Locate every Trypanosoma brucei.
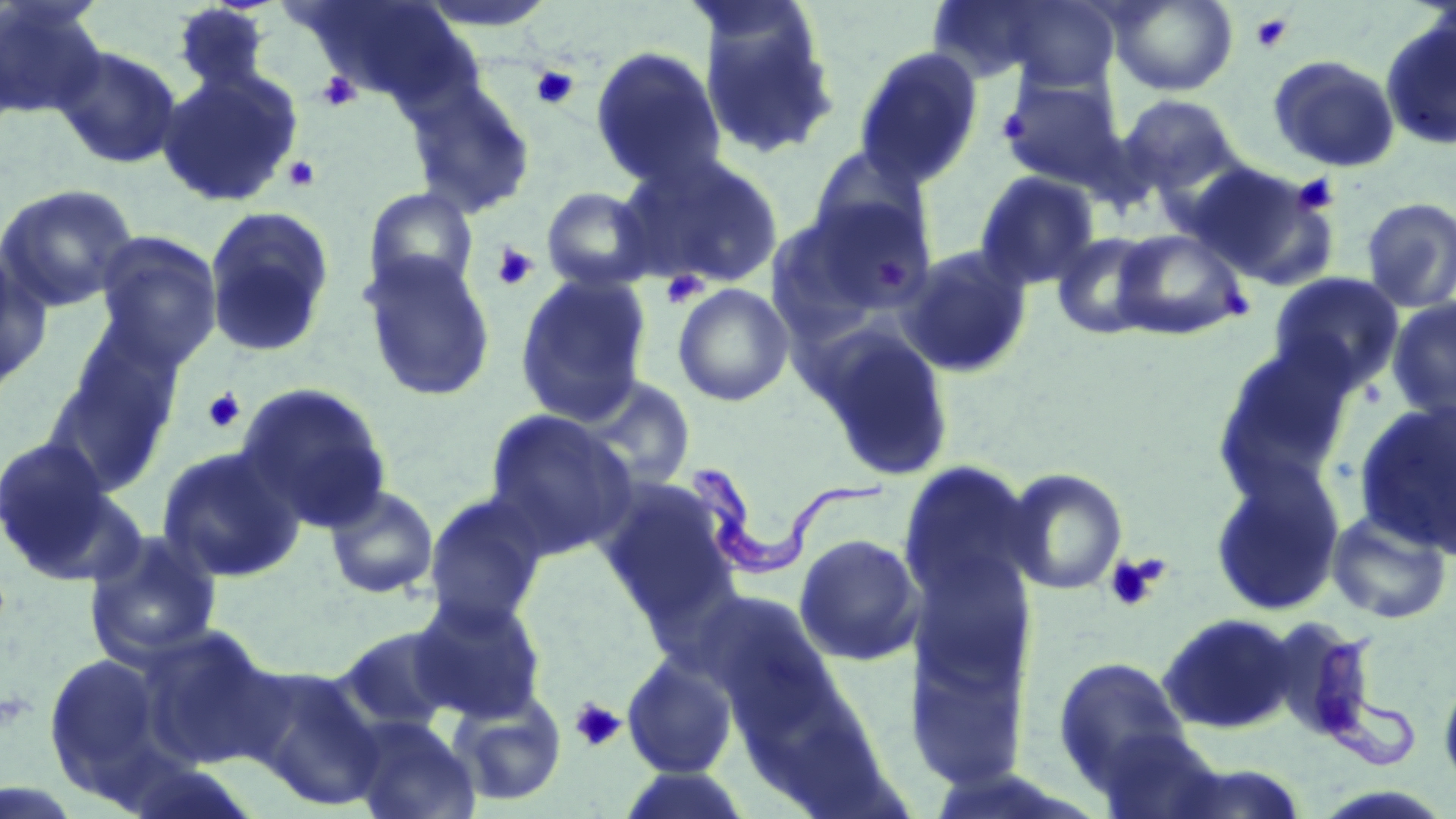

Approximate bounding boxes as [x1, y1, x2, y2] in pixels.
Trypanosoma brucei: [683, 461, 894, 573], [1309, 632, 1417, 772].

Uninfected red blood cell locations: [291, 0, 475, 105], [999, 0, 1120, 93], [1108, 0, 1238, 96], [0, 1, 108, 119], [924, 1, 1066, 85], [171, 3, 274, 95], [411, 3, 560, 32], [698, 11, 841, 162], [1379, 17, 1456, 151], [52, 44, 183, 170], [589, 45, 726, 188], [853, 45, 984, 188], [1267, 54, 1400, 173], [155, 68, 303, 208], [999, 74, 1127, 191], [405, 79, 537, 219], [1117, 94, 1242, 196], [802, 146, 932, 250], [617, 152, 785, 290], [1190, 164, 1341, 292], [973, 171, 1101, 291], [0, 183, 139, 313], [540, 186, 657, 293], [362, 187, 480, 299], [781, 194, 938, 324], [1360, 196, 1456, 313], [203, 205, 336, 359], [1112, 228, 1250, 340], [93, 230, 223, 369], [1051, 231, 1163, 339], [895, 244, 1034, 379], [0, 253, 53, 396], [359, 253, 497, 403], [1267, 272, 1404, 390], [514, 273, 653, 425], [672, 282, 795, 407], [1386, 297, 1456, 422], [56, 321, 186, 469], [807, 322, 957, 484], [1211, 342, 1357, 497], [572, 374, 697, 490], [235, 382, 392, 530], [1354, 400, 1455, 555], [483, 410, 638, 556], [0, 435, 123, 580], [156, 445, 306, 583], [898, 461, 1039, 615], [1208, 464, 1346, 618], [1002, 467, 1128, 596], [597, 481, 742, 628], [324, 484, 439, 599], [421, 490, 551, 628], [1326, 510, 1453, 625], [82, 528, 224, 667], [794, 533, 923, 666], [909, 546, 1035, 695], [693, 589, 831, 719], [408, 592, 548, 723], [1157, 613, 1298, 734], [334, 625, 466, 736], [134, 626, 283, 769], [42, 650, 174, 801], [1051, 655, 1196, 800], [622, 656, 738, 779], [243, 666, 385, 810], [1438, 673, 1456, 794], [448, 689, 568, 807], [348, 715, 480, 819], [615, 766, 754, 819]. Platelet locations: [1250, 11, 1295, 54], [530, 65, 580, 110], [316, 70, 361, 112], [997, 108, 1032, 146], [282, 155, 321, 192], [1291, 173, 1339, 215], [491, 243, 539, 290], [880, 261, 906, 288], [661, 271, 708, 309], [1223, 288, 1249, 319], [203, 388, 245, 434], [1104, 552, 1169, 614], [569, 697, 627, 752]. Slide-level diagnosis: Trypanosoma brucei. One field of a larger specimen. Light microscopy. Captured at 1000x magnification. Image is 1456×819 pixels. Thin blood smear. May-Grünwald-Giemsa stain.